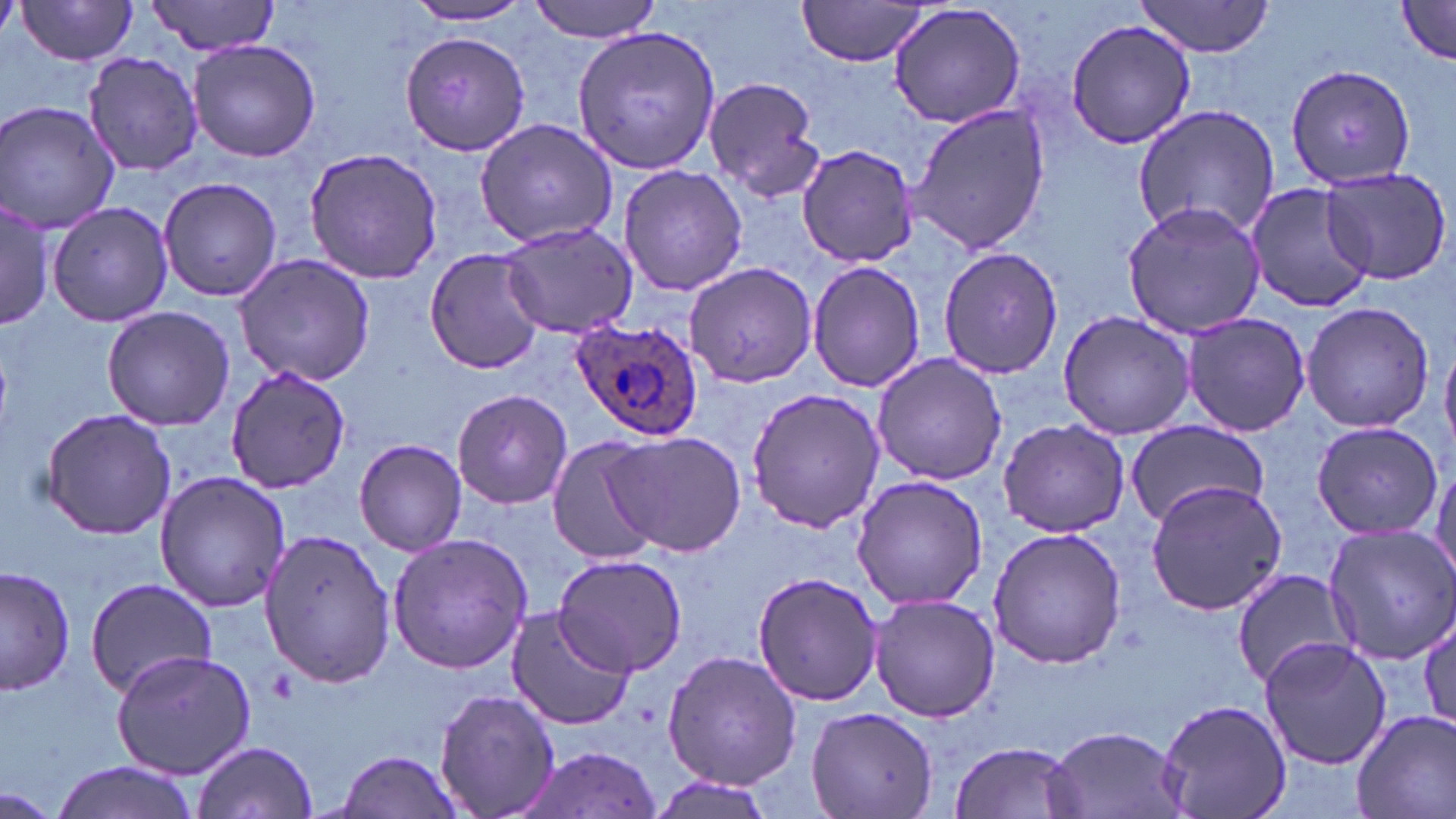

Plasmodium ovale-infected red blood cell locations = approximate bounding boxes as (x1, y1, x2, y2) in pixels: (571, 320, 705, 442)
slide-level diagnosis = Plasmodium ovale
uninfected red blood cell locations = approximate bounding boxes as (x1, y1, x2, y2) in pixels: (146, 0, 282, 57), (528, 0, 664, 42), (794, 0, 938, 68), (1134, 0, 1279, 58), (1393, 0, 1456, 68), (14, 1, 142, 65), (405, 3, 538, 25), (885, 3, 1028, 132), (1064, 19, 1199, 150), (572, 24, 721, 174), (401, 29, 531, 156), (186, 38, 322, 163), (80, 51, 204, 176), (1286, 64, 1418, 190), (702, 75, 825, 203), (1, 100, 121, 235), (904, 102, 1051, 256), (1133, 104, 1282, 243), (474, 116, 621, 248), (798, 143, 918, 268), (303, 147, 445, 283), (617, 163, 748, 297), (1319, 168, 1453, 285), (158, 176, 283, 301), (1244, 181, 1373, 314), (0, 197, 53, 332), (46, 199, 176, 326), (1121, 200, 1267, 339), (500, 221, 639, 339), (938, 246, 1063, 380), (425, 247, 549, 374), (230, 253, 377, 389), (684, 259, 817, 388), (806, 259, 926, 394), (1299, 301, 1435, 432), (101, 305, 236, 431), (1057, 309, 1196, 440), (1180, 312, 1311, 437), (1441, 339, 1456, 449), (871, 353, 1007, 485), (225, 367, 352, 493), (745, 385, 886, 534), (452, 387, 573, 508), (40, 408, 177, 540), (1124, 417, 1268, 528), (996, 419, 1131, 537), (1309, 421, 1442, 538), (606, 430, 745, 557), (545, 434, 665, 565), (354, 438, 469, 557), (1428, 458, 1456, 587), (155, 471, 292, 613), (850, 474, 989, 610), (1143, 478, 1287, 616), (1322, 523, 1456, 663), (988, 527, 1127, 670), (257, 529, 397, 686), (386, 533, 533, 674), (552, 553, 689, 677), (1, 564, 76, 697), (750, 569, 883, 707), (1231, 570, 1356, 688), (83, 578, 219, 698), (868, 592, 1001, 722), (503, 607, 636, 731), (1416, 612, 1454, 737), (1258, 636, 1392, 769), (111, 649, 257, 779), (661, 649, 803, 789), (433, 685, 559, 819), (1158, 697, 1291, 819), (806, 706, 939, 819), (1350, 707, 1456, 819), (1045, 725, 1188, 819), (190, 738, 319, 819), (949, 739, 1086, 819), (517, 746, 666, 818), (333, 749, 466, 819), (47, 761, 201, 819), (3, 788, 57, 816)
image size = 1456×819 pixels
stain = May-Grünwald-Giemsa
modality = optical microscopy
field of view = single
magnification = 1000x
preparation = thin blood smear